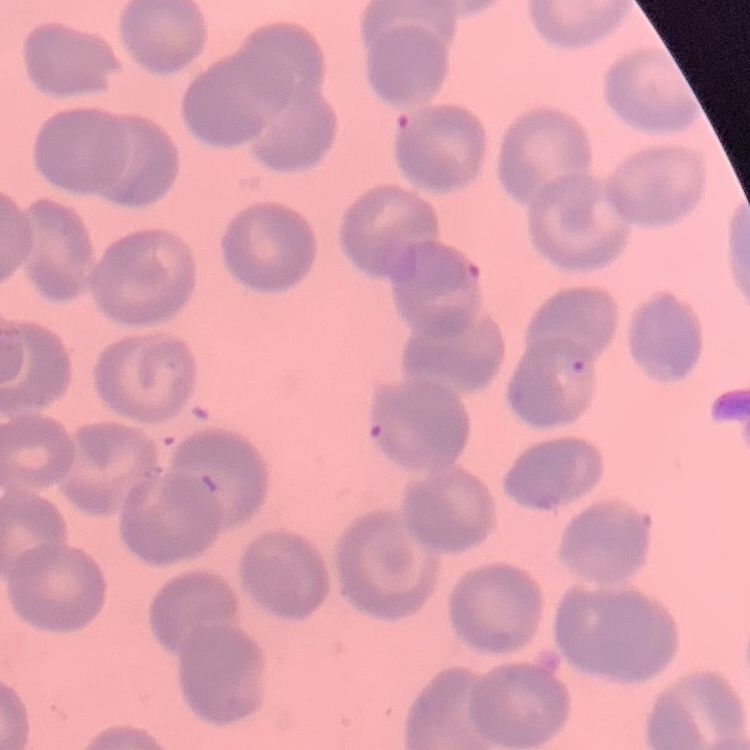

erythrocyte_morphology: no rouleaux formation
preparation: thin peripheral smear
stain: Field's or Giemsa
image_type: one tile cut from a larger photomicrograph